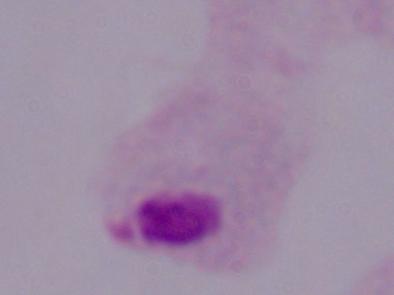
Captured at 1000x magnification. Micrograph. A trichomonad is shown.